Assess this cell for malaria.
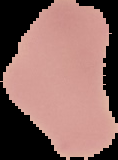
Uninfected.

image_size: 118×160 pixels
preparation: thin blood smear
image_type: segmented cell region on a black background